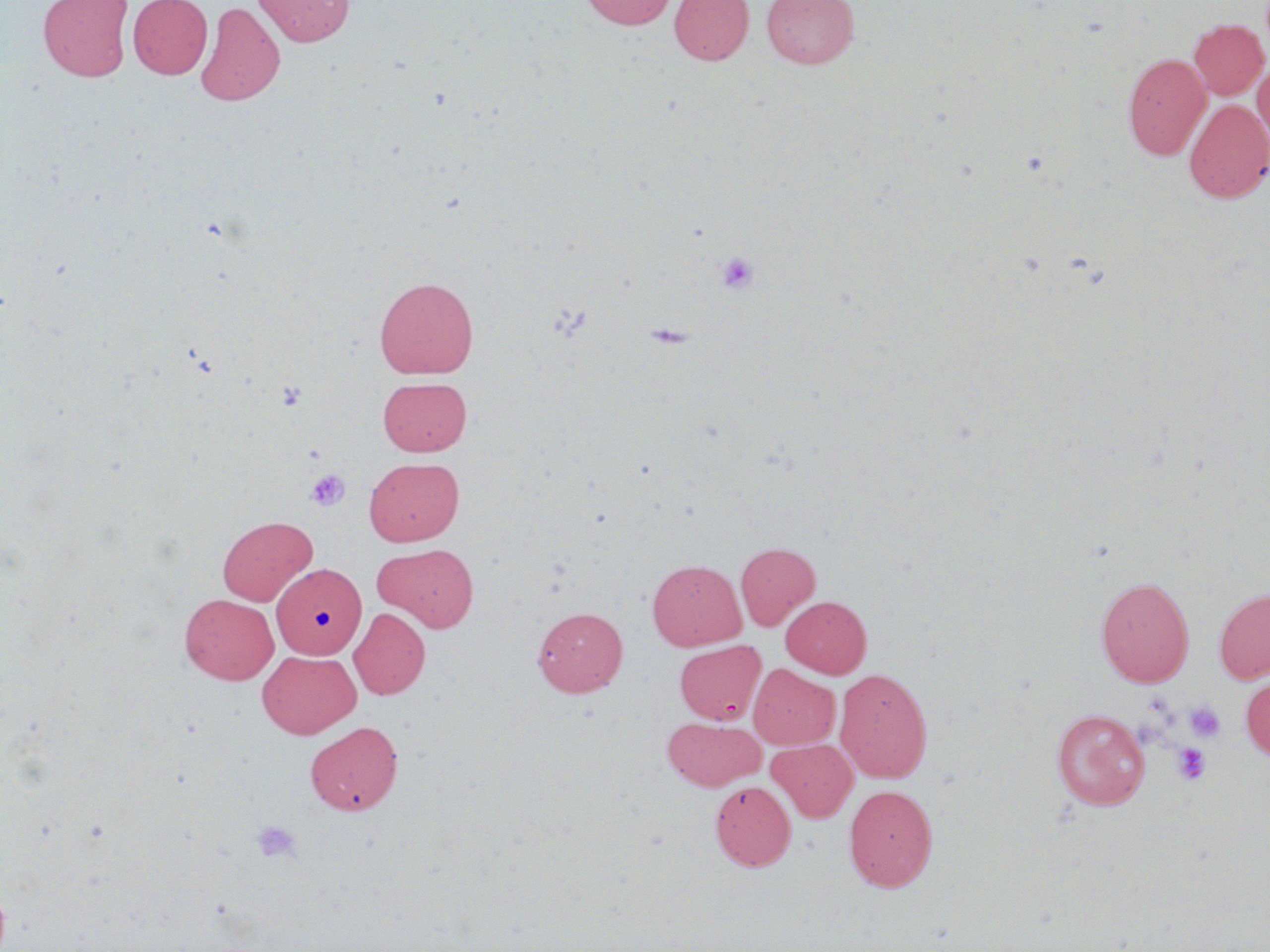 Approximate bounding boxes as [x1, y1, x2, y2] in pixels. Platelet locations: [714, 250, 761, 296], [275, 379, 308, 411], [305, 469, 350, 511], [1184, 701, 1226, 742], [1172, 743, 1211, 785], [252, 819, 301, 863]. Uninfected red blood cell locations: [38, 0, 133, 82], [128, 0, 213, 79], [253, 0, 355, 46], [578, 0, 677, 30], [669, 0, 754, 65], [761, 0, 860, 69], [195, 1, 285, 107], [1189, 18, 1269, 100], [1122, 52, 1211, 160], [1252, 60, 1270, 150], [1185, 98, 1270, 204], [374, 277, 478, 379], [378, 376, 472, 456], [364, 457, 465, 546], [217, 515, 317, 606], [735, 542, 820, 630], [374, 544, 479, 632], [647, 559, 747, 651], [273, 563, 366, 659], [1096, 577, 1194, 687], [1214, 588, 1270, 684], [180, 593, 279, 685], [781, 596, 872, 677], [533, 606, 628, 697], [348, 607, 430, 700], [679, 640, 770, 724], [258, 649, 360, 738], [749, 664, 840, 750], [834, 668, 933, 783], [1240, 673, 1270, 763], [1051, 709, 1150, 810], [663, 717, 765, 791], [305, 721, 403, 816], [767, 739, 858, 823], [710, 781, 796, 871], [844, 784, 938, 892]. Slide-level diagnosis: negative for blood parasites. Image is 1270×952 pixels. May-Grünwald-Giemsa-stained preparation. Thin blood smear. 1000x magnification. One field of a larger specimen. Optical microscopy.